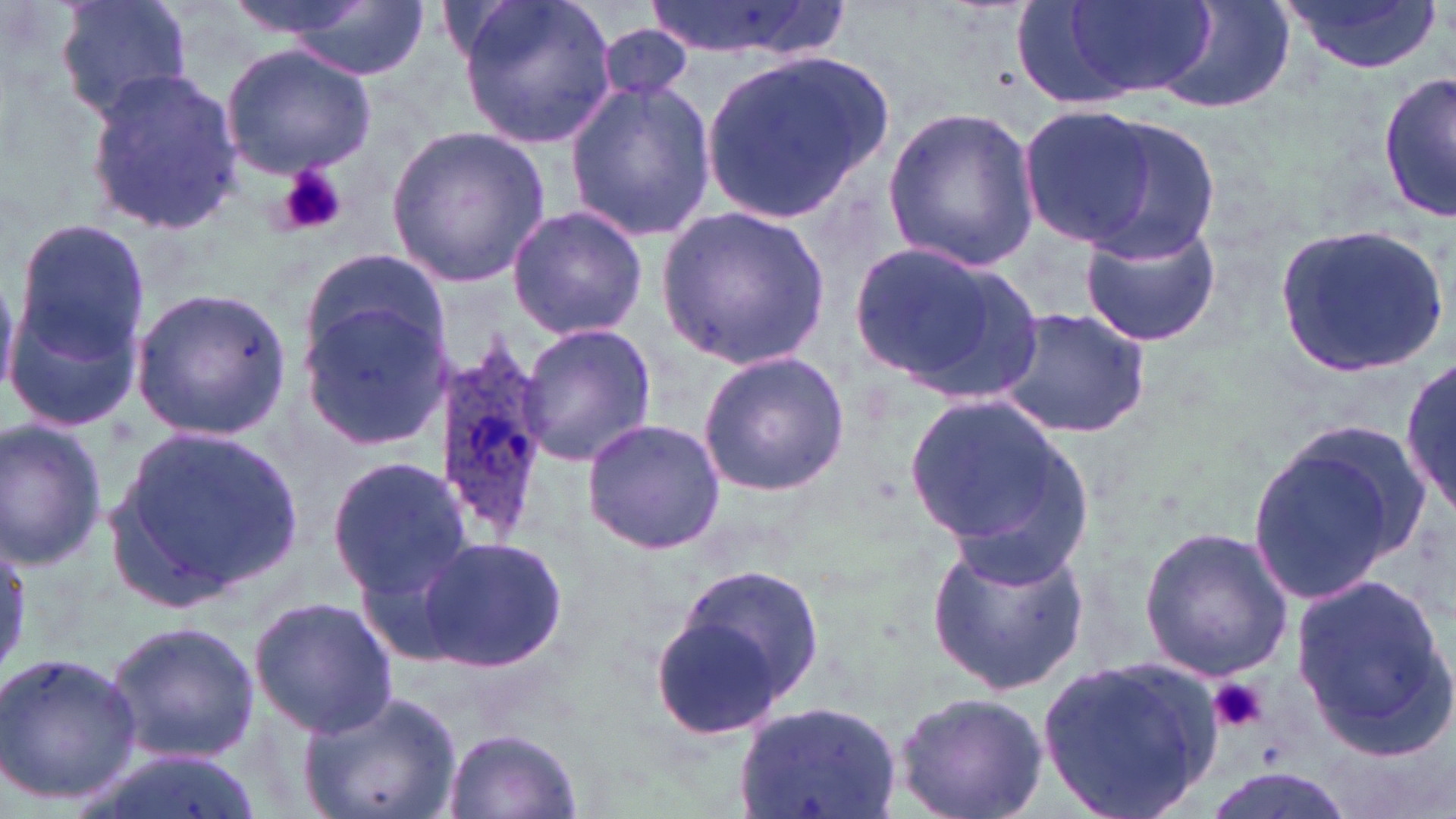
{
  "slide_level_diagnosis": "Plasmodium ovale",
  "uninfected_red_blood_cell_locations": "approximate bounding boxes as (x1,y1)-(x2,y2) corner pairs in pixels: (54,0)-(194,123), (221,0)-(381,42), (642,0)-(848,63), (454,1)-(619,149), (1155,1)-(1292,112), (1281,1)-(1443,76), (281,3)-(430,76), (1057,3)-(1216,102), (594,24)-(696,103), (221,44)-(378,177), (701,49)-(896,226), (82,68)-(244,235), (1379,69)-(1455,223), (564,80)-(716,241), (882,104)-(1039,271), (1015,104)-(1160,250), (1064,110)-(1226,263), (385,122)-(550,290), (505,205)-(647,340), (657,206)-(828,370), (9,217)-(150,373), (1079,220)-(1221,346), (1276,224)-(1452,378), (844,239)-(1040,398), (295,248)-(450,376), (132,285)-(293,440), (298,303)-(451,450), (993,307)-(1153,439), (516,322)-(658,469), (698,351)-(849,495), (1402,355)-(1454,523), (904,391)-(1094,576), (581,417)-(727,555), (0,420)-(108,571), (111,423)-(306,604), (1242,424)-(1433,609), (328,456)-(475,597), (1137,525)-(1293,680), (416,533)-(568,673), (925,538)-(1091,695), (663,565)-(825,726), (1290,570)-(1452,754), (248,595)-(397,738), (105,621)-(262,768), (0,647)-(143,811), (1037,656)-(1224,819), (299,689)-(463,819), (892,692)-(1050,819), (738,705)-(897,816), (441,729)-(583,819), (1199,771)-(1356,819)",
  "preparation": "thin blood film",
  "stain": "May-Grünwald-Giemsa",
  "modality": "optical microscopy",
  "field_of_view": "one of a larger specimen",
  "magnification": "1000x",
  "platelet_locations": "approximate bounding boxes as (x1,y1)-(x2,y2) corner pairs in pixels: (279,164)-(347,235), (1209,679)-(1269,735)",
  "image_size": "1456×819 pixels",
  "plasmodium_ovale_infected_red_blood_cell_locations": "approximate bounding boxes as (x1,y1)-(x2,y2) corner pairs in pixels: (434,338)-(553,544)"
}